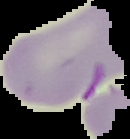
Result: malaria parasites detected. From a thin blood film. The area outside the segmented cell region is set to black. Image is 130×139 pixels.